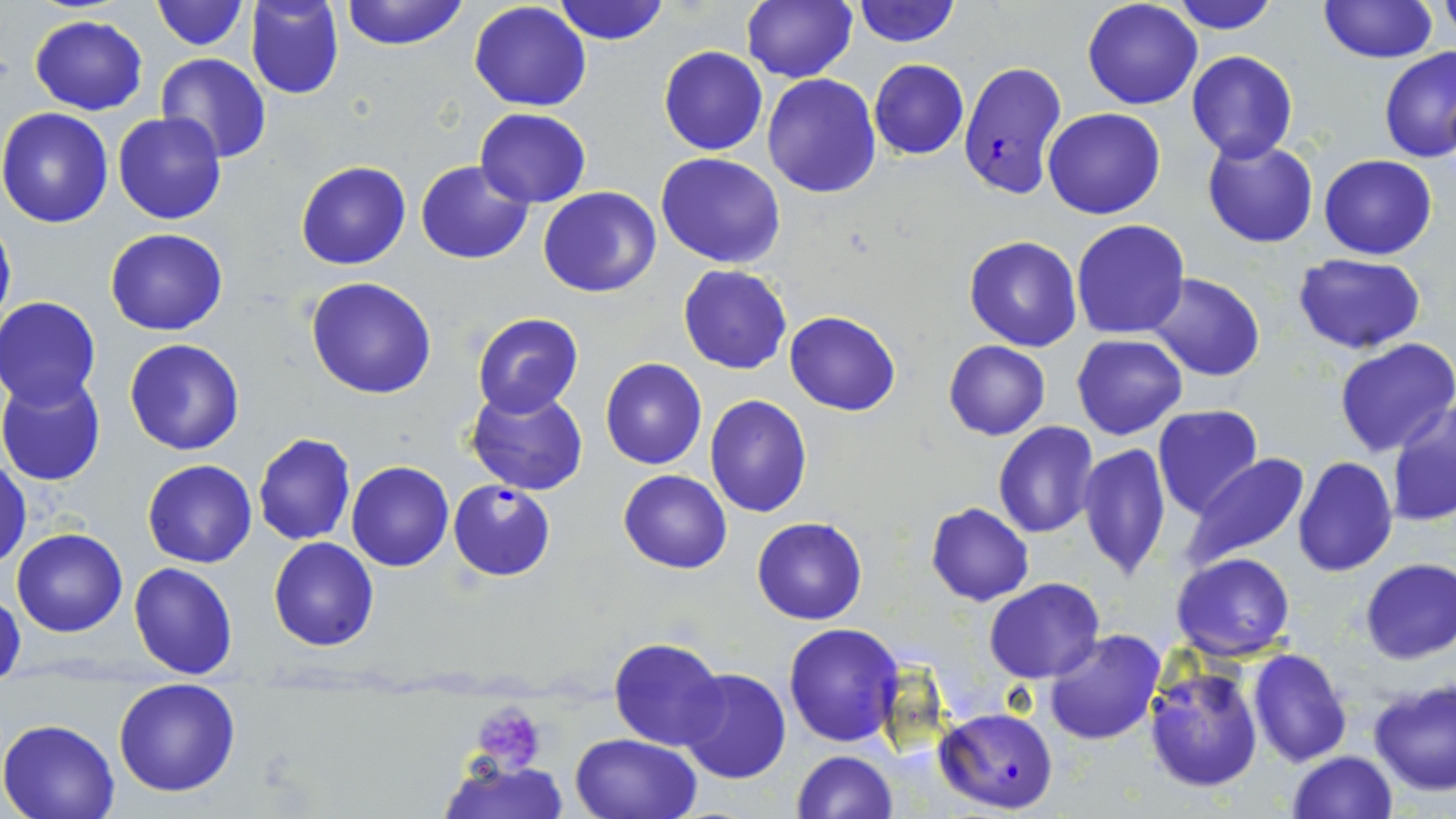
Summary:
  - Coordinate format: approximate bounding boxes as [x1, y1, x2, y2] in pixels
  - Platelet locations: [471, 699, 548, 775]
  - Plasmodium falciparum-infected red blood cell locations: [958, 59, 1068, 201], [447, 479, 556, 581], [936, 707, 1058, 813]
  - Uninfected red blood cell locations: [149, 0, 249, 50], [246, 0, 344, 100], [340, 0, 469, 50], [553, 0, 670, 45], [739, 0, 857, 83], [851, 0, 961, 47], [1081, 0, 1202, 109], [1167, 0, 1281, 33], [1319, 0, 1437, 64], [1437, 0, 1454, 50], [469, 2, 592, 111], [29, 15, 148, 114], [658, 46, 767, 156], [1380, 46, 1456, 162], [1187, 50, 1297, 162], [156, 52, 271, 163], [868, 59, 970, 160], [761, 73, 882, 199], [0, 107, 116, 228], [1042, 107, 1165, 219], [474, 108, 591, 207], [113, 112, 227, 225], [1202, 135, 1319, 248], [655, 152, 786, 269], [1319, 154, 1438, 259], [296, 160, 411, 270], [416, 160, 535, 265], [538, 186, 662, 297], [0, 215, 15, 341], [1070, 218, 1190, 339], [105, 228, 228, 336], [963, 236, 1083, 352], [1294, 254, 1425, 354], [678, 264, 792, 375], [1147, 272, 1267, 381], [305, 277, 438, 399], [0, 296, 102, 407], [785, 311, 901, 415], [470, 312, 585, 418], [1071, 335, 1187, 440], [1334, 337, 1456, 458], [125, 338, 244, 456], [944, 340, 1050, 440], [600, 357, 707, 469], [0, 373, 107, 487], [465, 384, 590, 496], [704, 393, 812, 518], [1386, 397, 1456, 529], [1152, 404, 1264, 518], [993, 421, 1099, 539], [253, 432, 356, 545], [143, 443, 356, 551], [1078, 443, 1172, 580], [0, 452, 30, 570], [1178, 453, 1310, 571], [1292, 455, 1397, 578], [142, 459, 257, 568], [346, 461, 453, 571], [619, 469, 731, 573], [926, 502, 1033, 605], [751, 517, 867, 624], [11, 528, 127, 636], [268, 537, 380, 652], [1171, 552, 1296, 660], [1359, 558, 1455, 664], [129, 562, 239, 679], [986, 578, 1105, 683], [0, 590, 25, 683], [783, 623, 904, 748], [1043, 629, 1167, 746], [608, 638, 727, 751], [1246, 649, 1351, 766], [1142, 663, 1264, 793], [678, 667, 792, 785], [112, 678, 241, 798], [1368, 679, 1456, 797], [0, 717, 120, 819], [570, 733, 701, 819], [791, 750, 899, 819], [1286, 751, 1397, 819], [437, 756, 569, 818]
  - Slide-level diagnosis: Plasmodium falciparum
  - Field of view: single
  - Magnification: 1000x
  - Image size: 1456×819 pixels
  - Modality: optical microscopy
  - Preparation: thin blood film
  - Stain: May-Grünwald-Giemsa